Locate every white blood cell.
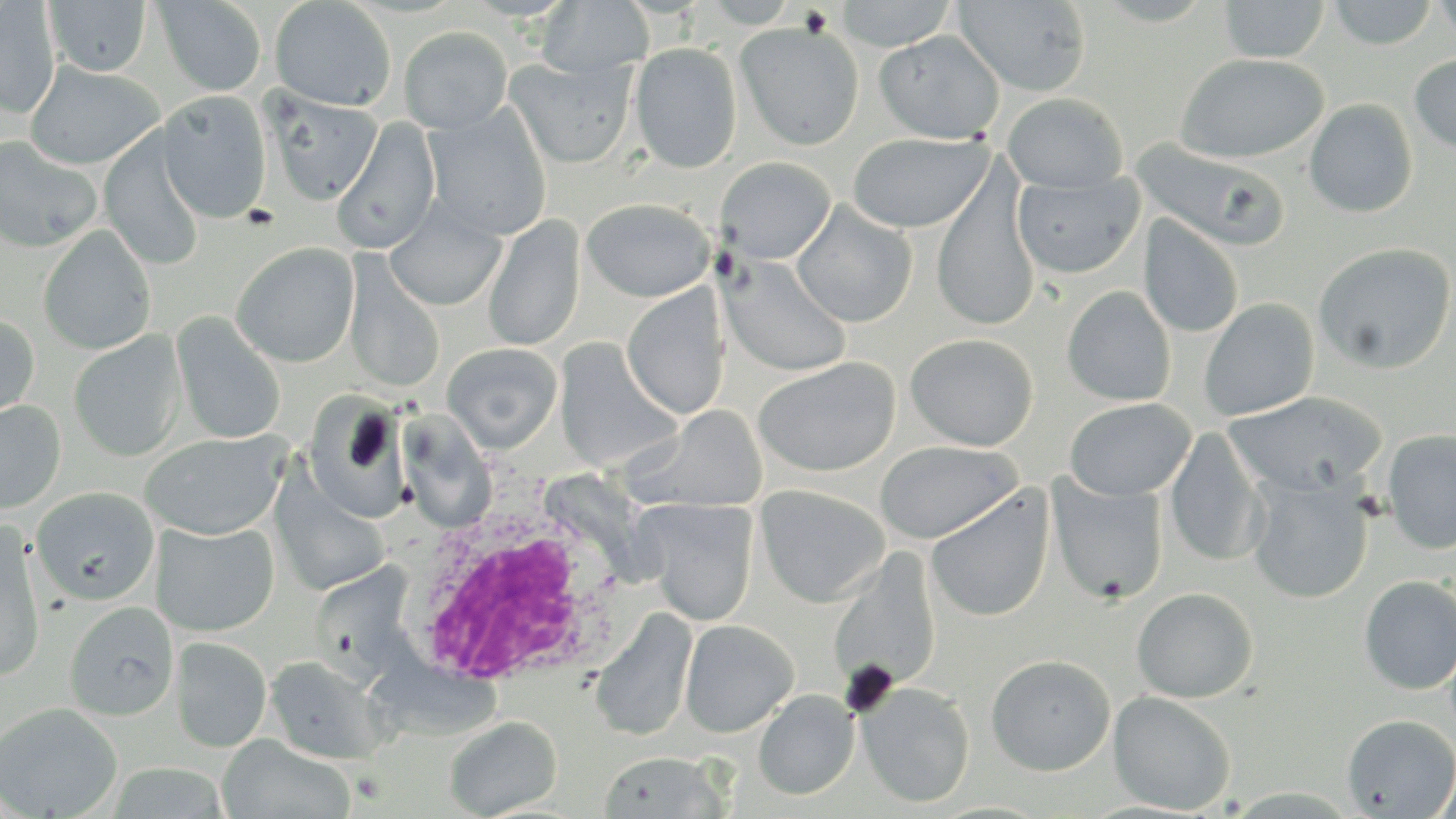

Approximate bounding boxes as [x1, y1, x2, y2] in pixels.
White blood cells: [400, 485, 633, 695].

slide-level diagnosis = Plasmodium ovale
magnification = 1000x
modality = optical microscopy
platelet locations = approximate bounding boxes as [x1, y1, x2, y2] in pixels: [841, 661, 898, 719]
field of view = one of a larger specimen
uninfected red blood cell locations = approximate bounding boxes as [x1, y1, x2, y2] in pixels: [270, 0, 396, 112], [836, 0, 958, 51], [953, 0, 1092, 96], [1218, 0, 1330, 62], [1327, 0, 1438, 49], [1431, 0, 1456, 43], [44, 1, 150, 77], [153, 1, 267, 96], [537, 1, 653, 77], [0, 2, 60, 117], [735, 20, 865, 151], [398, 25, 513, 134], [874, 29, 1005, 144], [630, 42, 742, 174], [1409, 52, 1456, 155], [1176, 53, 1328, 163], [506, 57, 636, 168], [24, 62, 164, 169], [156, 91, 273, 224], [265, 91, 383, 205], [1003, 92, 1128, 192], [1304, 98, 1418, 217], [422, 107, 553, 241], [330, 118, 442, 255], [99, 131, 206, 272], [847, 131, 993, 233], [0, 136, 102, 252], [1134, 140, 1289, 252], [715, 157, 836, 264], [932, 169, 1041, 332], [1013, 172, 1144, 279], [582, 198, 716, 302], [791, 201, 917, 328], [386, 203, 506, 312], [483, 215, 585, 352], [1139, 215, 1244, 338], [38, 225, 156, 355], [1313, 241, 1456, 374], [230, 242, 360, 367], [721, 257, 852, 377], [342, 261, 445, 394], [621, 285, 731, 421], [1062, 285, 1176, 406], [1199, 298, 1320, 421], [0, 311, 40, 426], [171, 311, 286, 445], [69, 330, 187, 462], [904, 333, 1038, 451], [555, 339, 681, 473], [442, 342, 563, 453], [753, 356, 901, 477], [1223, 392, 1387, 497], [302, 394, 412, 523], [1064, 397, 1196, 501], [0, 400, 66, 514], [630, 406, 769, 513], [1164, 428, 1267, 566], [1382, 428, 1456, 555], [139, 431, 288, 540], [874, 439, 1023, 544], [1047, 475, 1169, 605], [1246, 475, 1373, 603], [271, 476, 391, 595], [755, 484, 891, 607], [31, 486, 159, 606], [926, 486, 1054, 622], [638, 499, 759, 626], [0, 519, 46, 681], [153, 520, 280, 636], [829, 552, 941, 693], [1358, 574, 1456, 694], [1132, 587, 1258, 703], [65, 601, 179, 720], [590, 609, 698, 740], [680, 619, 799, 737], [171, 636, 271, 752], [986, 654, 1116, 776], [265, 655, 389, 764], [857, 681, 975, 808], [754, 689, 859, 800], [1108, 691, 1236, 814], [0, 702, 123, 818], [1342, 713, 1456, 817], [444, 715, 563, 818], [217, 735, 356, 819], [597, 751, 731, 818], [106, 762, 231, 819], [1433, 762, 1456, 819]
preparation = thin blood film
stain = May-Grünwald-Giemsa
image size = 1456×819 pixels